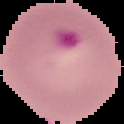

image_type: segmented cell region with the area outside set to black
preparation: thin blood smear
result: Plasmodium parasites detected
image_size: 124×124 pixels